Classify this cell by malaria status.
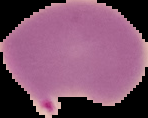
Parasitized.

Cell region segmented out of the field of view; the surrounding area is masked to black. Image is 148×118 pixels. From a thin blood smear.